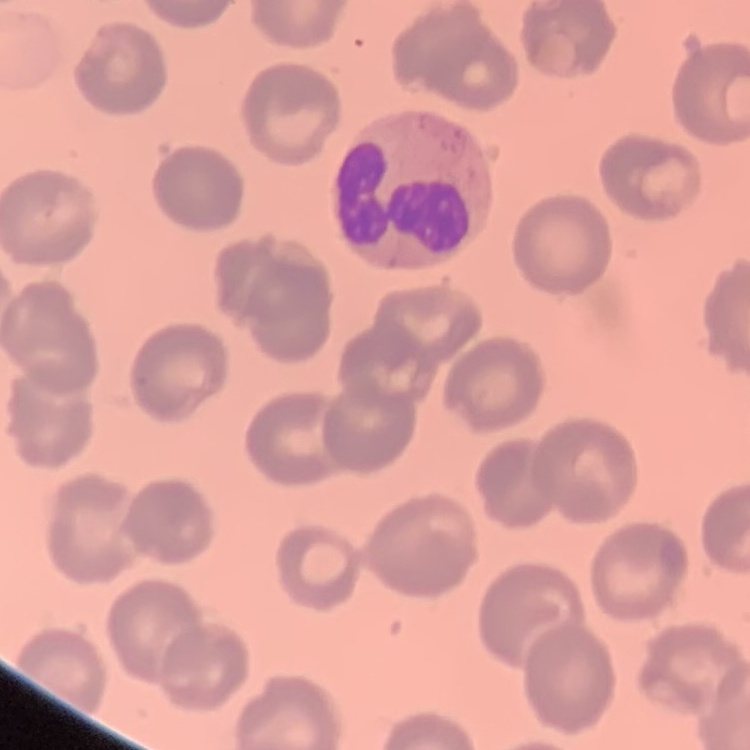
The red blood cells show no rouleaux formation. Thin blood film. Square crop of a larger photomicrograph. Stained with either Field's or Giemsa.